Assess this cell for malaria.
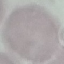
Uninfected.

Summary:
  - Image type: automatically extracted cell patch, resized to 64 × 64 pixels
  - Preparation: thin smear
  - Capture: smartphone through the microscope eyepiece
  - Stain: Giemsa